Give the position of every Plasmodium parasite visible.
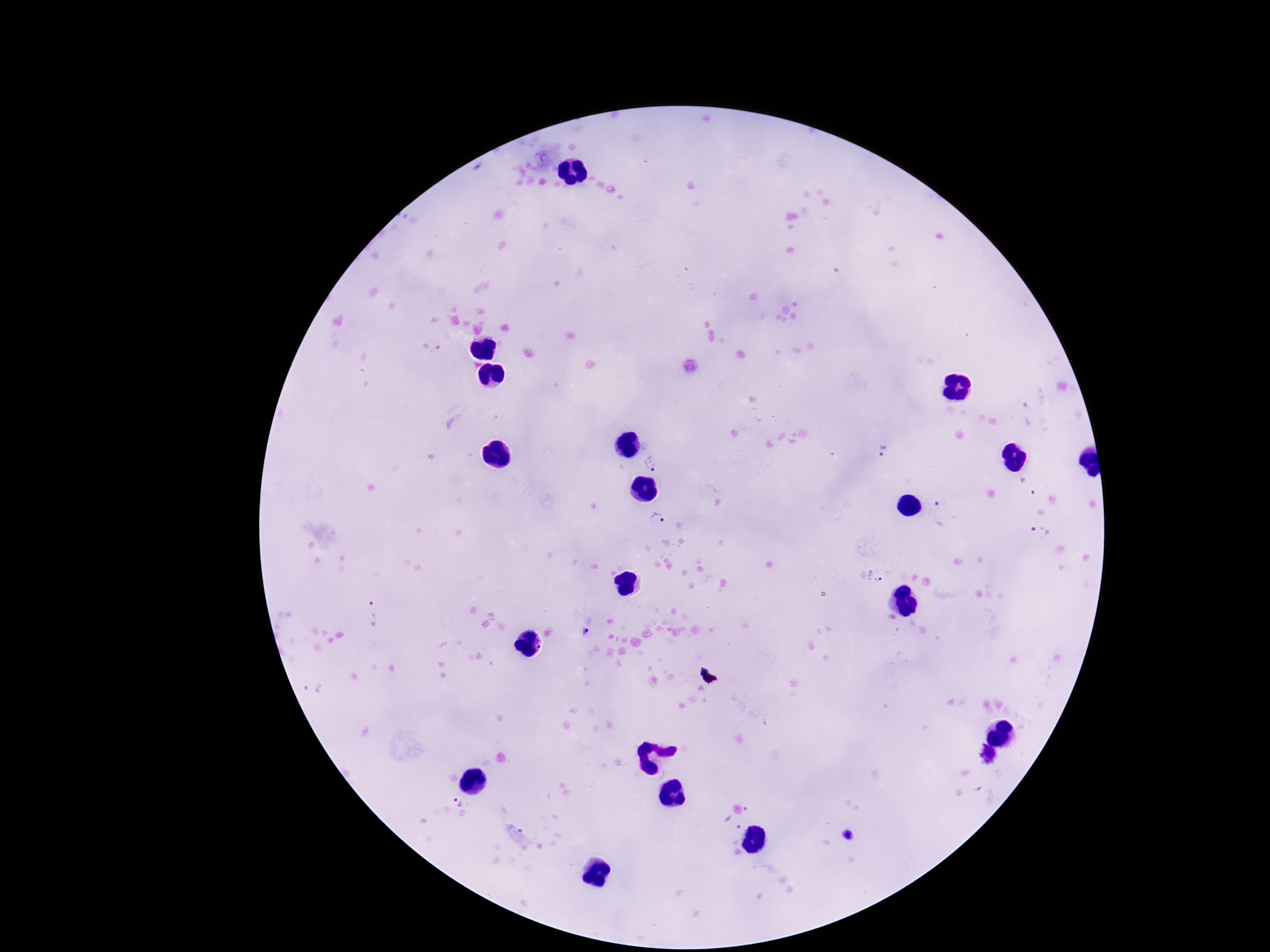

Approximate centers as (x, y) in pixels.
Plasmodium parasites: (431, 348), (1028, 416), (886, 451), (654, 461), (1027, 488), (941, 515), (657, 518), (1039, 533), (871, 577), (371, 613), (585, 631), (314, 687), (459, 803).

Thick blood film. 100x magnification. One field from this slide. Giemsa-stained preparation. Smartphone photograph taken through the microscope eyepiece. Image is 1270×952 pixels. Patient malaria status: infected.